Locate every blood parasite and identify its species.
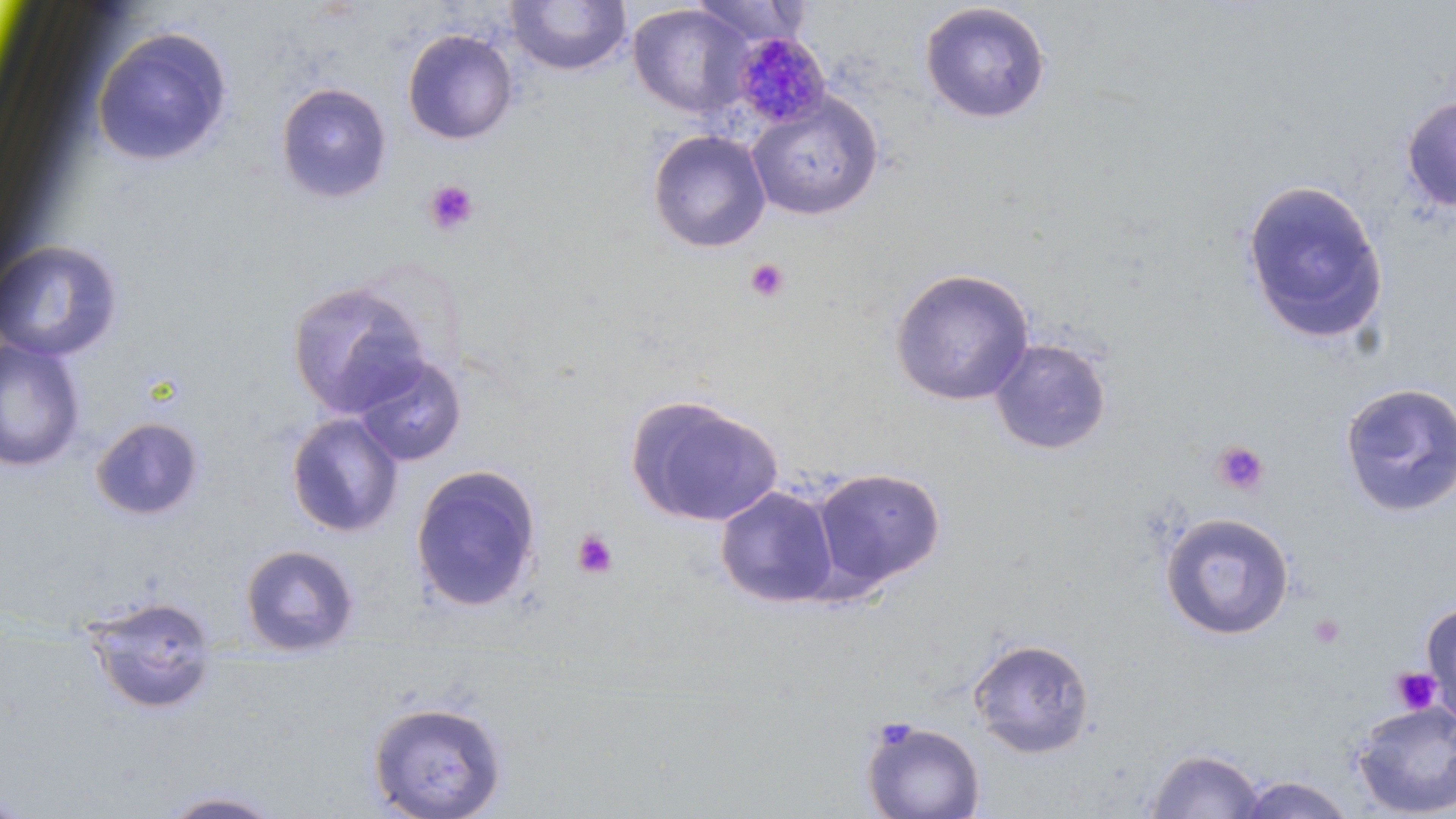

Approximate bounding boxes as (x1, y1, x2, y2) in pixels.
Plasmodium malariae-infected red blood cells: (732, 32, 831, 128).
No Plasmodium falciparum, Plasmodium ovale, Plasmodium vivax, Babesia divergens, or Trypanosoma brucei observed.

{
  "slide_level_diagnosis": "Plasmodium malariae",
  "platelet_locations": "approximate bounding boxes as (x1, y1, x2, y2) in pixels: (424, 180, 479, 236), (745, 258, 791, 302), (1212, 441, 1269, 496), (572, 529, 619, 580), (1308, 613, 1345, 649), (1390, 667, 1441, 715)",
  "modality": "optical microscopy",
  "image_size": "1456×819 pixels",
  "magnification": "1000x",
  "field_of_view": "one of a larger specimen",
  "uninfected_red_blood_cell_locations": "approximate bounding boxes as (x1, y1, x2, y2) in pixels: (505, 0, 631, 77), (688, 1, 808, 48), (919, 2, 1051, 124), (627, 3, 753, 119), (91, 26, 233, 167), (402, 28, 518, 145), (275, 82, 393, 203), (745, 91, 884, 221), (1401, 95, 1456, 213), (648, 130, 772, 253), (1240, 178, 1389, 345), (0, 240, 123, 363), (890, 268, 1035, 406), (286, 279, 432, 418), (1, 337, 87, 473), (989, 337, 1112, 456), (351, 354, 467, 467), (1339, 382, 1456, 518), (626, 394, 784, 528), (285, 413, 405, 537), (89, 416, 205, 522), (409, 463, 542, 613), (810, 467, 946, 592), (715, 485, 840, 609), (1159, 512, 1295, 641), (238, 543, 361, 657), (82, 595, 220, 717), (1420, 600, 1456, 726), (967, 637, 1095, 759), (367, 700, 508, 819), (1351, 701, 1455, 817), (861, 718, 985, 819), (1143, 746, 1266, 818), (1231, 774, 1357, 818), (156, 789, 291, 819)",
  "stain": "May-Grünwald-Giemsa",
  "preparation": "thin blood film"
}